Assess this cell for malaria.
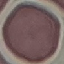
It is uninfected.

preparation = thin blood smear
image type = cell patch, automatically extracted from a larger field of view and resized to 64 × 64 pixels
capture = smartphone through the microscope eyepiece
stain = Giemsa